Name the parasite shown.
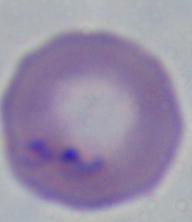
Babesia.

modality = photomicrograph
magnification = 1000x